Assess this cell for malaria.
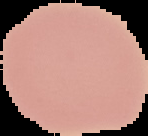

It is uninfected.

Summary:
  - Preparation: thin blood smear
  - Image size: 148×136 pixels
  - Image type: segmented cell region with the area outside set to black